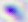
Summary:
  - Magnification: 400x
  - Modality: photomicrograph
  - Identification: Toxoplasma gondii